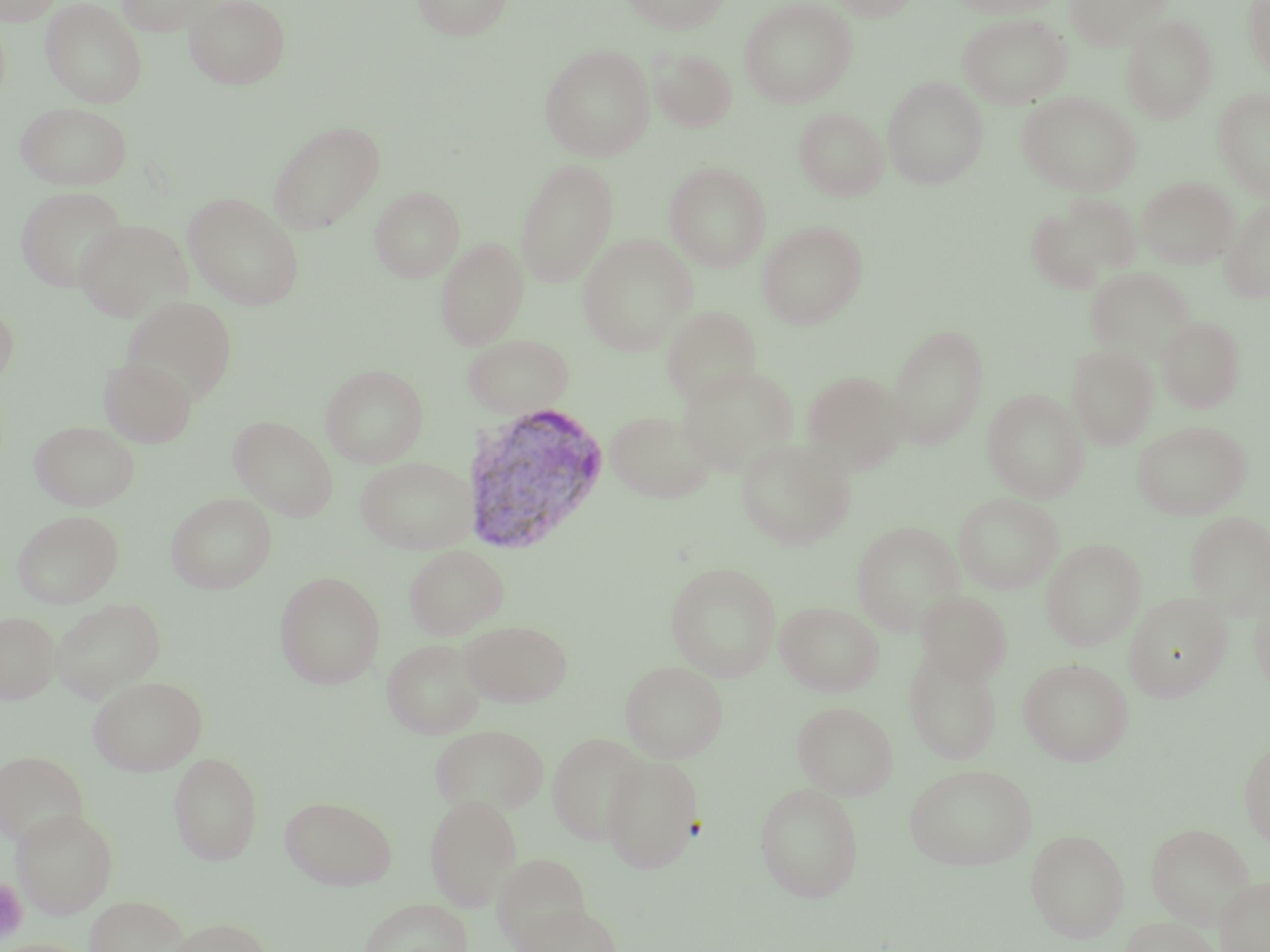
slide-level diagnosis = Plasmodium vivax
field of view = single
Plasmodium vivax-infected red blood cell locations = approximate bounding boxes as (x1,y1)-(x2,y2) corner pairs in pixels: (461,401)-(612,555)
magnification = 1000x
platelet locations = approximate bounding boxes as (x1,y1)-(x2,y2) corner pairs in pixels: (0,878)-(28,943)
stain = May-Grünwald-Giemsa
uninfected red blood cell locations = approximate bounding boxes as (x1,y1)-(x2,y2) corner pairs in pixels: (0,0)-(63,26), (116,0)-(219,36), (185,0)-(291,88), (411,0)-(514,40), (622,0)-(731,33), (739,0)-(857,108), (826,0)-(921,20), (947,0)-(1066,17), (1064,0)-(1172,50), (40,1)-(148,108), (1243,1)-(1270,78), (958,13)-(1072,108), (1122,14)-(1218,123), (540,45)-(655,161), (649,48)-(736,132), (883,75)-(988,189), (1213,87)-(1270,201), (1017,92)-(1142,195), (16,102)-(132,190), (794,107)-(889,200), (268,119)-(387,235), (515,158)-(618,287), (665,162)-(771,271), (1137,177)-(1237,269), (16,186)-(129,292), (371,186)-(463,282), (183,192)-(304,309), (1026,194)-(1140,291), (1220,198)-(1270,302), (73,219)-(191,321), (757,220)-(868,329), (577,234)-(697,355), (436,237)-(529,350), (1085,267)-(1195,362), (122,295)-(238,405), (0,299)-(19,390), (661,305)-(761,406), (1157,316)-(1245,412), (887,323)-(988,449), (463,333)-(575,418), (1067,343)-(1158,450), (99,356)-(197,448), (321,364)-(428,468), (676,364)-(800,477), (801,370)-(907,474), (983,389)-(1089,503), (606,409)-(716,504), (229,416)-(338,520), (29,420)-(140,511), (1132,420)-(1251,520), (736,437)-(856,549), (356,456)-(478,553), (167,493)-(277,593), (953,493)-(1063,593), (12,510)-(124,608), (1185,511)-(1270,617), (851,521)-(965,635), (1041,539)-(1145,650), (404,544)-(509,639), (666,561)-(781,681), (274,571)-(386,689), (1249,580)-(1270,701), (915,590)-(1012,685), (1123,592)-(1232,702), (51,598)-(166,702), (776,601)-(884,696), (1,610)-(61,704), (459,619)-(573,707), (382,638)-(487,739), (905,646)-(1002,765), (1018,657)-(1133,766), (620,661)-(728,762), (89,674)-(207,775), (793,701)-(898,799), (429,723)-(549,816), (547,732)-(650,845), (1239,738)-(1270,850), (0,750)-(88,849), (168,750)-(264,866), (601,754)-(704,873), (904,763)-(1037,871), (754,783)-(864,902), (425,793)-(522,911), (280,795)-(397,890), (11,808)-(118,918), (1146,822)-(1255,927), (1025,828)-(1129,943), (492,852)-(591,949), (1215,876)-(1270,952), (84,893)-(190,952), (359,897)-(473,952), (513,902)-(626,952), (1120,916)-(1223,952), (165,917)-(274,952)
preparation = thin blood smear
modality = light microscopy
image size = 1270×952 pixels